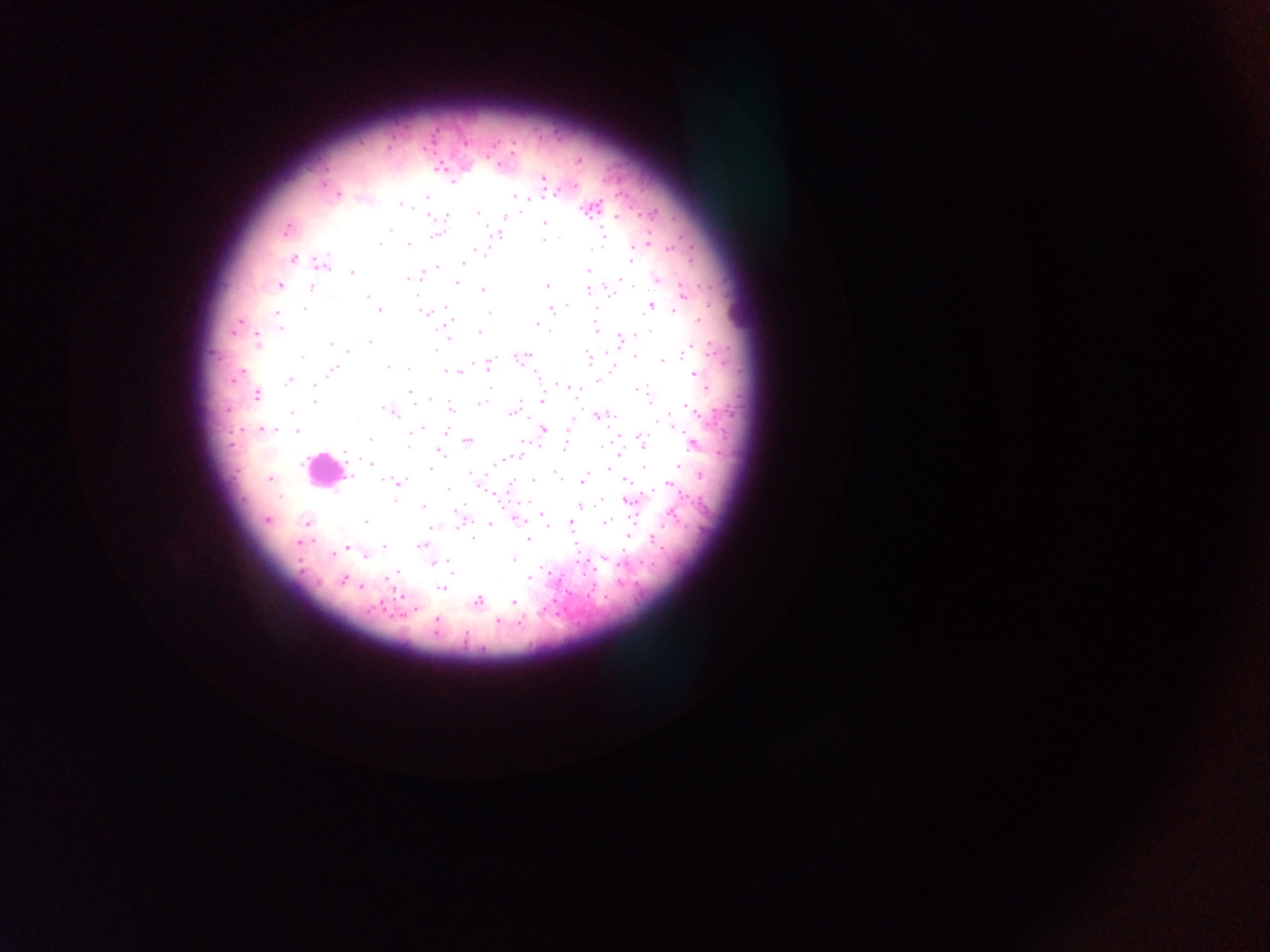 Approximate centers as x y in pixels. Plasmodium parasite locations: 578 159; 440 167; 543 179; 452 181; 572 187; 336 193; 427 195; 513 195; 400 203; 590 208; 478 212; 428 215; 504 216; 615 216; 446 217; 544 224; 287 228; 496 234; 437 235; 544 242; 647 242; 377 244; 409 244; 670 248; 591 249; 631 258; 294 259; 465 262; 321 264; 438 266; 589 272; 353 273; 421 275; 413 277; 656 279; 457 282; 279 285; 547 286; 589 288; 610 288; 311 289; 481 290; 683 293; 367 296; 651 305; 568 306; 551 308; 379 310; 427 313; 488 313; 276 314; 449 320; 237 323; 536 323; 279 328; 448 328; 595 328; 479 332; 257 341; 369 342; 620 342; 330 344; 347 351; 634 355; 521 357; 589 359; 663 360; 487 365; 387 368; 408 368; 330 371; 456 371; 694 374; 290 379; 598 379; 567 387; 409 391; 256 395; 314 399; 541 399; 483 401; 450 410; 513 411; 389 412; 599 415; 672 425; 543 428; 262 429; 297 432; 368 440; 467 441; 641 441; 693 442; 565 444; 407 448; 440 450; 618 454; 514 456; 369 463; 432 470; 270 479; 583 479; 624 479; 534 480; 398 482; 479 483; 668 483; 446 488; 497 493; 631 501; 424 506; 581 506; 542 512; 461 517; 515 518; 267 519; 365 521; 570 521; 605 521; 306 523; 489 524; 431 525; 547 525; 628 536; 472 537; 528 539; 298 542; 423 545; 384 546; 347 547; 512 559; 447 560; 433 562; 529 575; 342 580; 441 589; 478 600; 513 602; 436 621; 497 622. Leukocyte locations: 323 470. Image is 1270×952 pixels. Sample from Ghana. Thick blood smear. Single field of view. Photographed through a microscope with a mobile-phone camera.